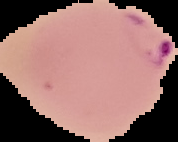
preparation = thin blood film
malaria status = parasitized
image size = 178×142 pixels
image type = cell region segmented out of the field of view; surrounding area masked to black